Describe the morphology of the erythrocytes.
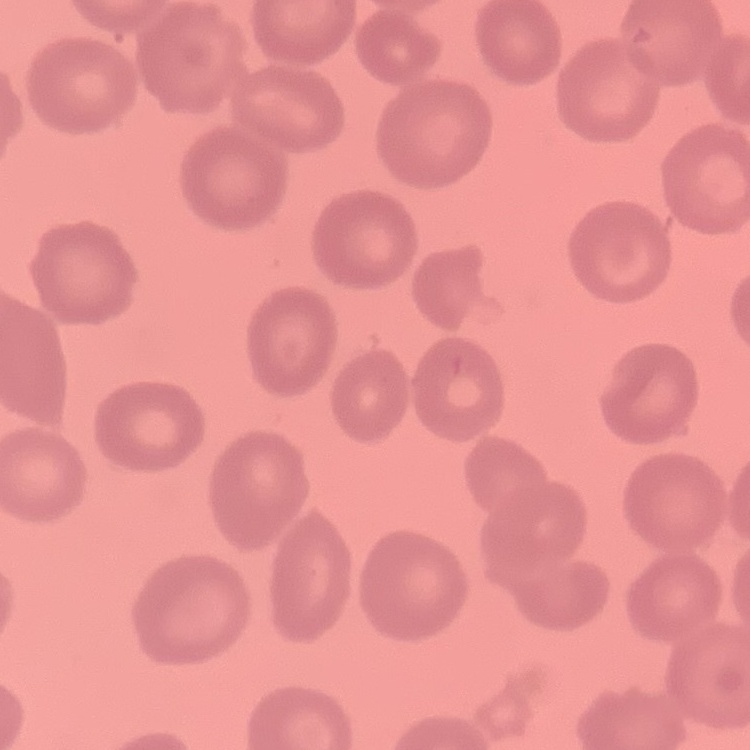

They show no rouleaux formation.

preparation = thin peripheral smear
image type = one tile cut from a larger photomicrograph
stain = Field's or Giemsa